State which parasite is depicted.
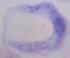

This is a trypanosome.

Summary:
  - Modality: photomicrograph
  - Magnification: 1000x